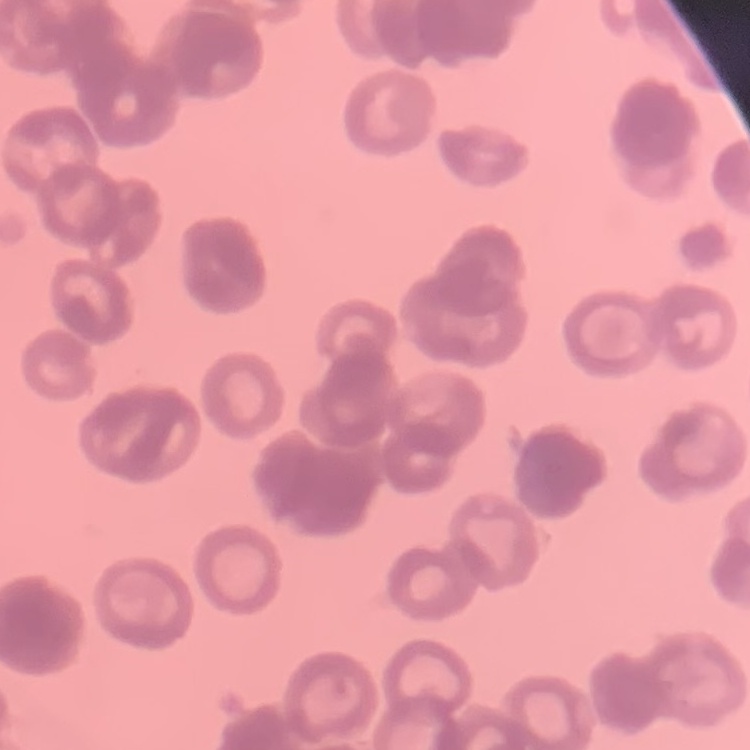

erythrocyte_morphology: rouleaux formation
image_type: square crop of a larger photomicrograph
preparation: thin blood smear
stain: Field's or Giemsa